Locate every blood parasite and identify its species.
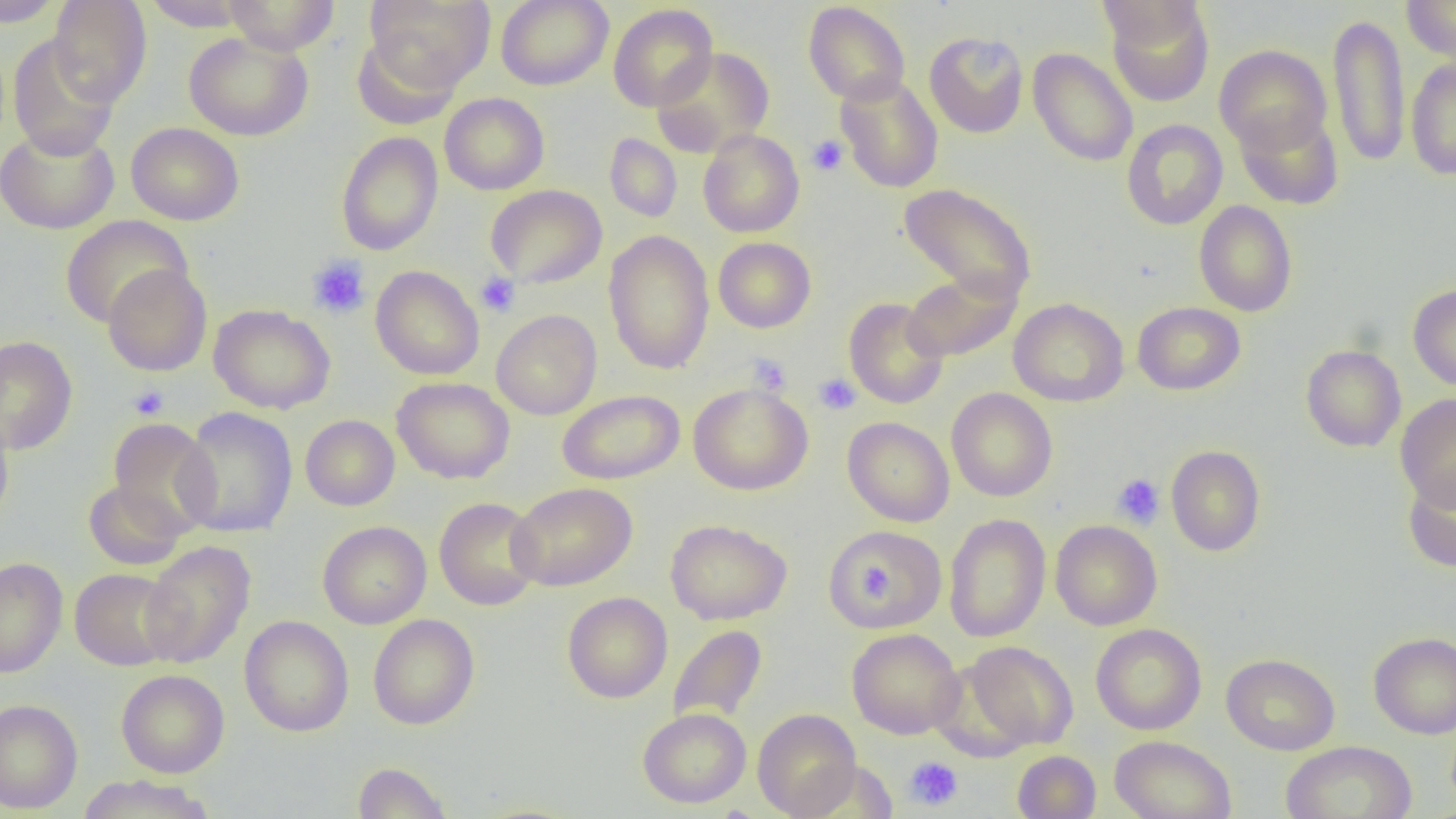

No blood parasites seen.

Approximate bounding boxes as named x1/y1/x2/y2 corners in pixels. Platelet locations: (x1=806, y1=135, x2=849, y2=176), (x1=307, y1=254, x2=370, y2=319), (x1=476, y1=272, x2=520, y2=316), (x1=747, y1=354, x2=792, y2=396), (x1=813, y1=373, x2=861, y2=415), (x1=128, y1=384, x2=169, y2=420), (x1=1112, y1=474, x2=1165, y2=528), (x1=858, y1=561, x2=897, y2=601), (x1=903, y1=756, x2=963, y2=811). Uninfected red blood cell locations: (x1=1, y1=0, x2=67, y2=27), (x1=223, y1=0, x2=340, y2=55), (x1=364, y1=0, x2=494, y2=90), (x1=496, y1=0, x2=613, y2=90), (x1=1095, y1=0, x2=1206, y2=48), (x1=1401, y1=0, x2=1456, y2=61), (x1=48, y1=1, x2=152, y2=106), (x1=143, y1=1, x2=251, y2=31), (x1=803, y1=1, x2=910, y2=105), (x1=1104, y1=1, x2=1215, y2=106), (x1=608, y1=3, x2=718, y2=112), (x1=1328, y1=12, x2=1410, y2=168), (x1=924, y1=31, x2=1029, y2=138), (x1=184, y1=32, x2=314, y2=141), (x1=351, y1=32, x2=462, y2=130), (x1=7, y1=35, x2=119, y2=160), (x1=1214, y1=45, x2=1332, y2=155), (x1=651, y1=47, x2=774, y2=157), (x1=1027, y1=47, x2=1138, y2=167), (x1=1406, y1=58, x2=1456, y2=180), (x1=835, y1=74, x2=944, y2=193), (x1=439, y1=92, x2=549, y2=194), (x1=1235, y1=107, x2=1343, y2=210), (x1=1121, y1=119, x2=1228, y2=230), (x1=126, y1=122, x2=244, y2=226), (x1=0, y1=126, x2=119, y2=234), (x1=698, y1=130, x2=804, y2=237), (x1=336, y1=132, x2=443, y2=256), (x1=604, y1=133, x2=682, y2=222), (x1=898, y1=183, x2=1037, y2=304), (x1=485, y1=184, x2=607, y2=289), (x1=1193, y1=200, x2=1298, y2=317), (x1=60, y1=215, x2=193, y2=327), (x1=603, y1=230, x2=715, y2=375), (x1=713, y1=237, x2=816, y2=333), (x1=102, y1=263, x2=212, y2=376), (x1=370, y1=265, x2=484, y2=380), (x1=902, y1=269, x2=1021, y2=363), (x1=1408, y1=283, x2=1456, y2=391), (x1=843, y1=298, x2=948, y2=409), (x1=1009, y1=298, x2=1129, y2=406), (x1=1132, y1=301, x2=1245, y2=395), (x1=208, y1=304, x2=335, y2=414), (x1=491, y1=309, x2=602, y2=420), (x1=0, y1=335, x2=78, y2=454), (x1=1300, y1=344, x2=1406, y2=452), (x1=392, y1=377, x2=514, y2=484), (x1=688, y1=382, x2=813, y2=495), (x1=947, y1=387, x2=1058, y2=502), (x1=557, y1=390, x2=685, y2=485), (x1=1395, y1=394, x2=1456, y2=509), (x1=176, y1=406, x2=298, y2=538), (x1=300, y1=414, x2=400, y2=510), (x1=0, y1=415, x2=14, y2=529), (x1=842, y1=416, x2=954, y2=527), (x1=106, y1=418, x2=220, y2=537), (x1=1166, y1=445, x2=1266, y2=556), (x1=1402, y1=469, x2=1456, y2=573), (x1=83, y1=480, x2=188, y2=569), (x1=507, y1=482, x2=637, y2=591), (x1=434, y1=497, x2=543, y2=610), (x1=943, y1=514, x2=1051, y2=643), (x1=665, y1=519, x2=791, y2=625), (x1=1050, y1=520, x2=1162, y2=630), (x1=317, y1=521, x2=431, y2=629), (x1=823, y1=525, x2=947, y2=632), (x1=140, y1=540, x2=255, y2=668), (x1=0, y1=557, x2=68, y2=679), (x1=70, y1=567, x2=180, y2=670), (x1=562, y1=592, x2=672, y2=703), (x1=368, y1=614, x2=480, y2=730), (x1=239, y1=615, x2=354, y2=736), (x1=1091, y1=623, x2=1206, y2=735), (x1=668, y1=624, x2=767, y2=727), (x1=847, y1=627, x2=964, y2=739), (x1=1368, y1=632, x2=1456, y2=739), (x1=960, y1=640, x2=1078, y2=751), (x1=1221, y1=653, x2=1339, y2=755), (x1=116, y1=669, x2=229, y2=777), (x1=0, y1=699, x2=83, y2=812), (x1=637, y1=708, x2=752, y2=808), (x1=752, y1=708, x2=862, y2=818), (x1=1110, y1=735, x2=1237, y2=819), (x1=1280, y1=740, x2=1417, y2=819), (x1=1012, y1=750, x2=1101, y2=819), (x1=351, y1=761, x2=453, y2=818), (x1=78, y1=774, x2=215, y2=819). Slide-level diagnosis: negative for blood parasites. One field of a larger specimen. Thin blood smear. Image is 1456×819 pixels. Light microscopy. 1000x magnification.